Point out each Plasmodium parasite.
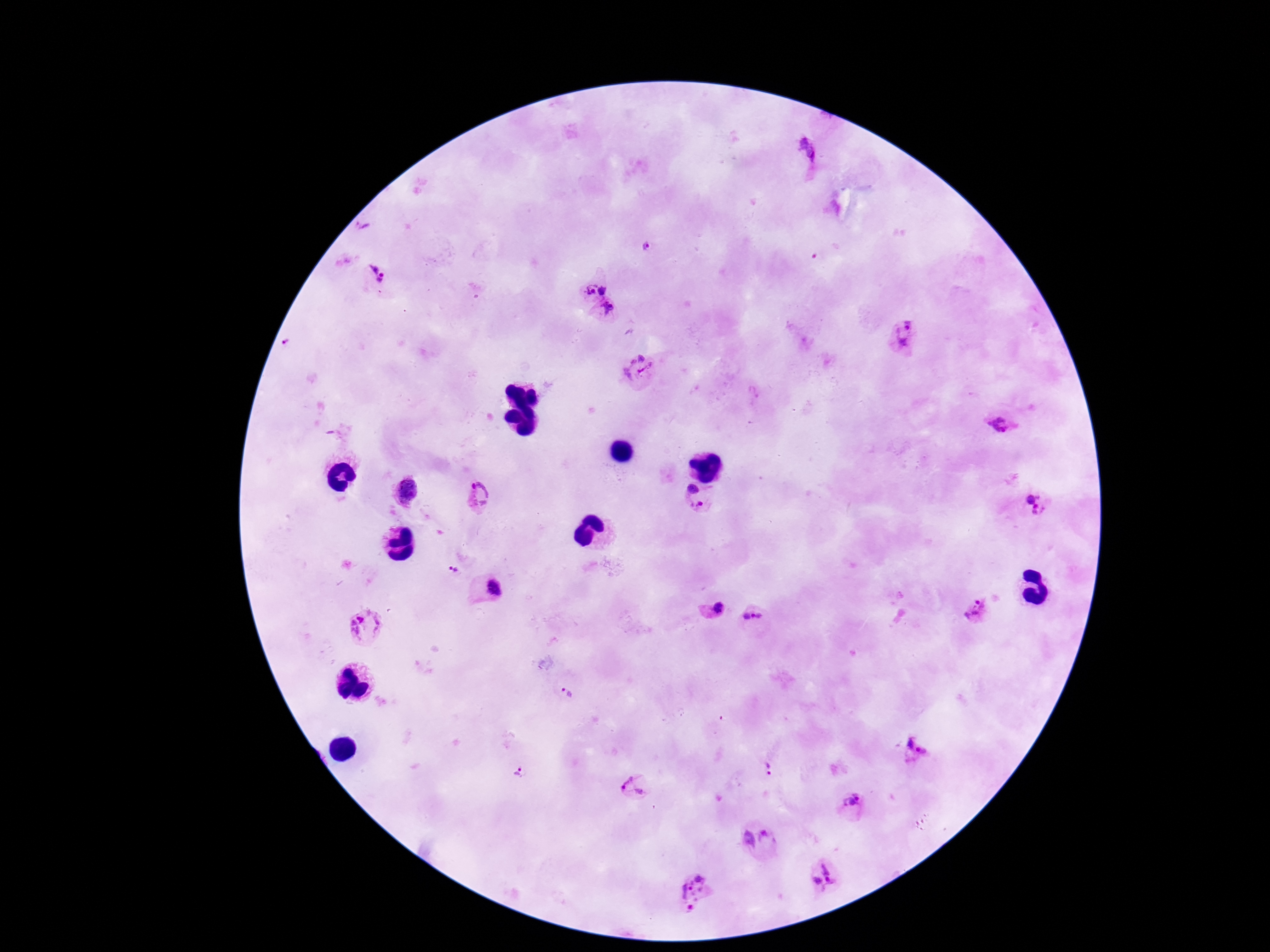

Approximate centers as {x, y} in pixels.
Plasmodium parasites: {803, 153}, {363, 229}, {645, 246}, {375, 275}, {589, 289}, {604, 291}, {609, 311}, {903, 336}, {289, 343}, {639, 371}, {1001, 424}, {693, 491}, {406, 492}, {480, 494}, {1037, 504}, {699, 508}, {453, 569}, {491, 587}, {718, 609}, {975, 610}, {752, 617}, {366, 627}, {566, 691}, {914, 751}, {769, 767}, {520, 773}, {634, 787}, {852, 805}, {757, 839}, {823, 876}, {694, 892}.

{
  "magnification": "100x",
  "image_size": "1270×952 pixels",
  "capture": "smartphone camera through the microscope eyepiece",
  "field_of_view": "single",
  "preparation": "thick blood smear",
  "stain": "Giemsa",
  "patient_malaria_status": "infected"
}